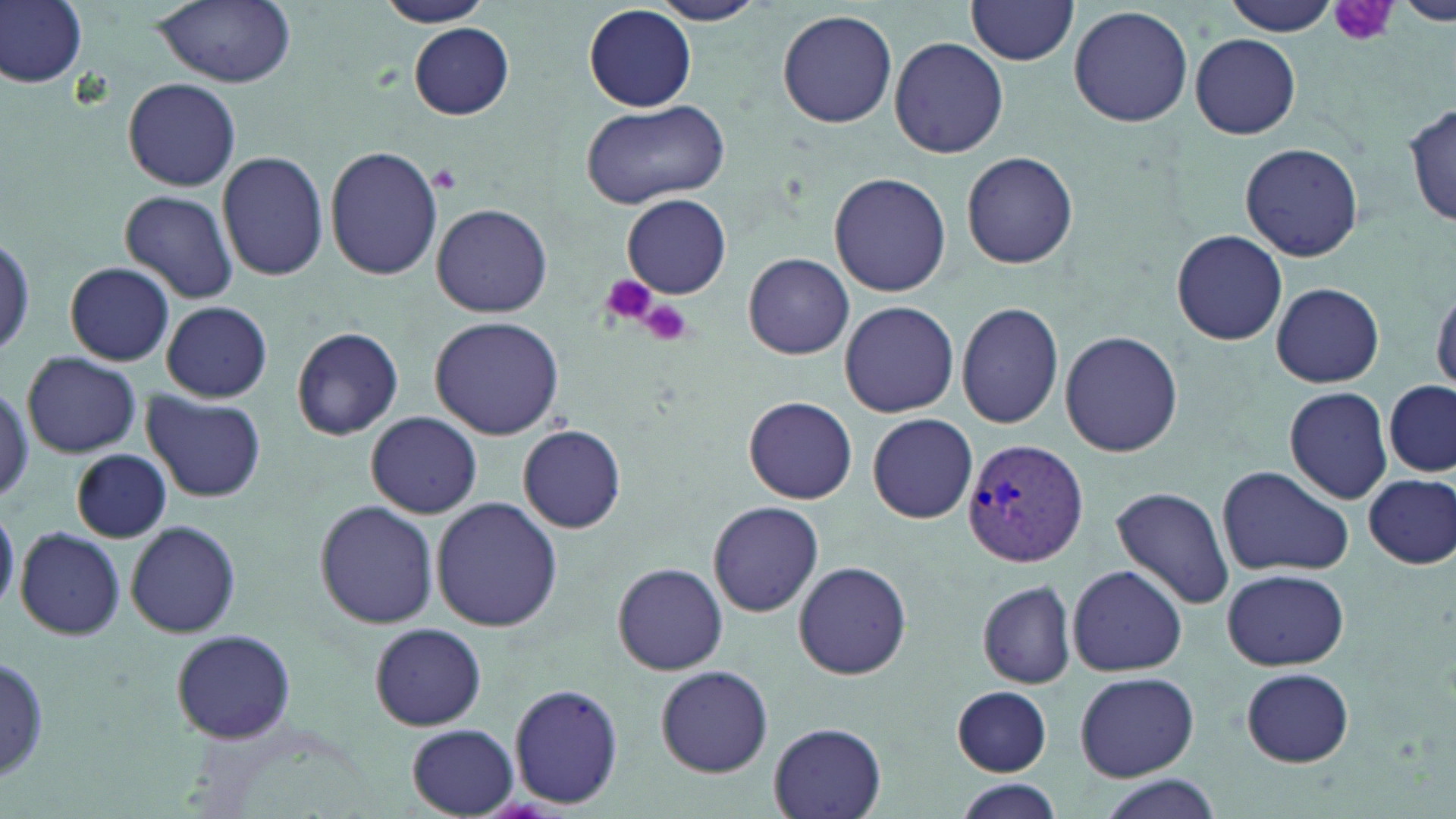

Approximate bounding boxes as named x1/y1/x2/y2 corners in pixels. Uninfected red blood cell locations: (x1=1, y1=0, x2=88, y2=90), (x1=150, y1=0, x2=297, y2=88), (x1=372, y1=0, x2=493, y2=27), (x1=649, y1=0, x2=768, y2=25), (x1=1227, y1=0, x2=1340, y2=37), (x1=966, y1=1, x2=1079, y2=66), (x1=1398, y1=1, x2=1456, y2=25), (x1=1068, y1=5, x2=1195, y2=128), (x1=585, y1=6, x2=696, y2=112), (x1=778, y1=9, x2=898, y2=130), (x1=409, y1=23, x2=514, y2=121), (x1=1189, y1=33, x2=1301, y2=140), (x1=890, y1=36, x2=1010, y2=159), (x1=123, y1=75, x2=241, y2=191), (x1=582, y1=101, x2=731, y2=208), (x1=1404, y1=101, x2=1456, y2=228), (x1=1240, y1=142, x2=1364, y2=260), (x1=325, y1=146, x2=444, y2=282), (x1=218, y1=150, x2=328, y2=282), (x1=961, y1=150, x2=1078, y2=270), (x1=828, y1=172, x2=951, y2=297), (x1=120, y1=190, x2=240, y2=305), (x1=622, y1=195, x2=731, y2=297), (x1=432, y1=204, x2=553, y2=317), (x1=1171, y1=229, x2=1287, y2=346), (x1=743, y1=253, x2=855, y2=359), (x1=66, y1=262, x2=174, y2=365), (x1=1429, y1=282, x2=1456, y2=398), (x1=1271, y1=283, x2=1384, y2=387), (x1=838, y1=300, x2=959, y2=418), (x1=162, y1=301, x2=273, y2=402), (x1=955, y1=302, x2=1065, y2=429), (x1=430, y1=316, x2=564, y2=440), (x1=289, y1=326, x2=405, y2=441), (x1=1059, y1=330, x2=1183, y2=459), (x1=21, y1=352, x2=140, y2=459), (x1=1385, y1=381, x2=1456, y2=478), (x1=1282, y1=387, x2=1391, y2=504), (x1=144, y1=392, x2=265, y2=502), (x1=743, y1=396, x2=858, y2=504), (x1=366, y1=412, x2=481, y2=518), (x1=867, y1=414, x2=978, y2=523), (x1=518, y1=425, x2=627, y2=534), (x1=71, y1=449, x2=172, y2=542), (x1=1215, y1=466, x2=1352, y2=577), (x1=1359, y1=471, x2=1455, y2=569), (x1=1110, y1=485, x2=1235, y2=611), (x1=432, y1=498, x2=562, y2=632), (x1=706, y1=501, x2=826, y2=616), (x1=314, y1=502, x2=438, y2=628), (x1=0, y1=506, x2=19, y2=612), (x1=126, y1=520, x2=241, y2=639), (x1=15, y1=529, x2=126, y2=639), (x1=792, y1=558, x2=912, y2=680), (x1=612, y1=562, x2=728, y2=675), (x1=1067, y1=563, x2=1186, y2=677), (x1=1222, y1=567, x2=1348, y2=671), (x1=975, y1=579, x2=1079, y2=690), (x1=368, y1=623, x2=487, y2=729), (x1=170, y1=630, x2=296, y2=744), (x1=0, y1=650, x2=50, y2=788), (x1=656, y1=665, x2=773, y2=777), (x1=1237, y1=666, x2=1356, y2=765), (x1=1074, y1=671, x2=1198, y2=781), (x1=509, y1=682, x2=626, y2=810), (x1=948, y1=683, x2=1056, y2=778), (x1=769, y1=723, x2=887, y2=818), (x1=406, y1=724, x2=518, y2=817), (x1=1091, y1=777, x2=1220, y2=819), (x1=952, y1=780, x2=1064, y2=819). Plasmodium vivax-infected red blood cell locations: (x1=961, y1=440, x2=1092, y2=569). Platelet locations: (x1=1327, y1=0, x2=1396, y2=47), (x1=429, y1=167, x2=461, y2=192), (x1=598, y1=273, x2=658, y2=328), (x1=638, y1=299, x2=694, y2=346). Slide-level diagnosis: Plasmodium vivax. Optical microscopy. One field of a larger specimen. May-Grünwald-Giemsa stain. Image is 1456×819 pixels. Captured at 1000x magnification. Thin blood film.